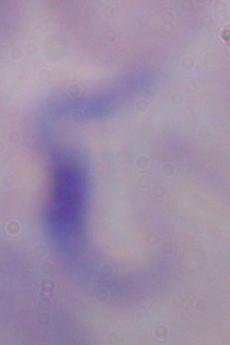
Summary:
  - Magnification: 1000x
  - Modality: micrograph
  - Identification: trypanosome